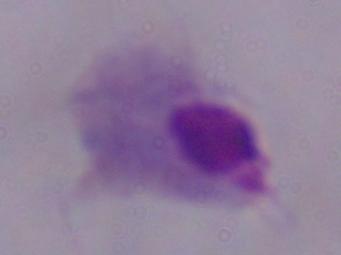
Summary:
  - Identification: trichomonad
  - Modality: micrograph
  - Magnification: 1000x